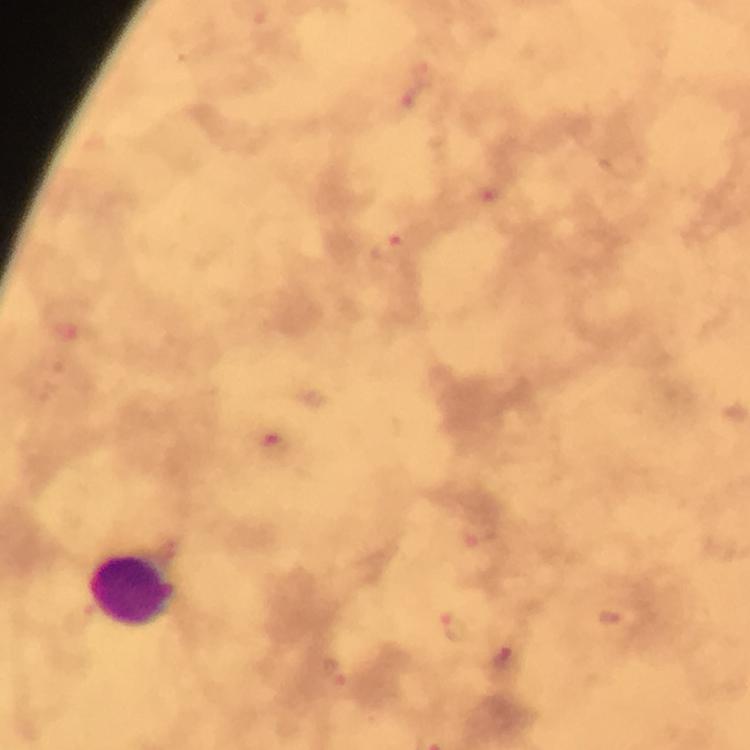 Approximate centers as {x, y} in pixels. Malaria parasite locations: {416, 95}, {485, 197}, {387, 247}, {274, 442}, {478, 537}, {611, 618}, {456, 626}, {506, 663}, {343, 683}. Leukocyte locations: {133, 592}. 100x magnification. A crop from one field of view. Giemsa stain. From a diagnostic examination for malaria. Immersion oil was used. Photographed through the microscope with a smartphone camera. Thick smear. Image is 750×750 pixels.